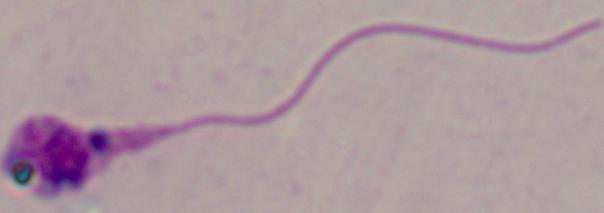
A Leishmania parasite is shown. 1000x magnification. Micrograph.